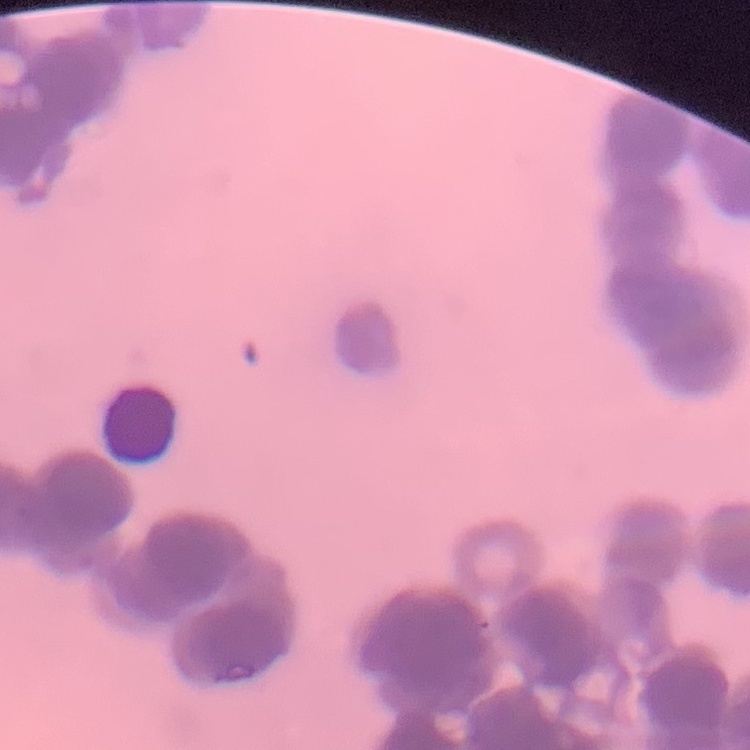

Summary:
  - Red blood cell morphology: rouleaux formation
  - Stain: Field's or Giemsa
  - Image type: square crop of a larger photomicrograph
  - Preparation: thin blood film